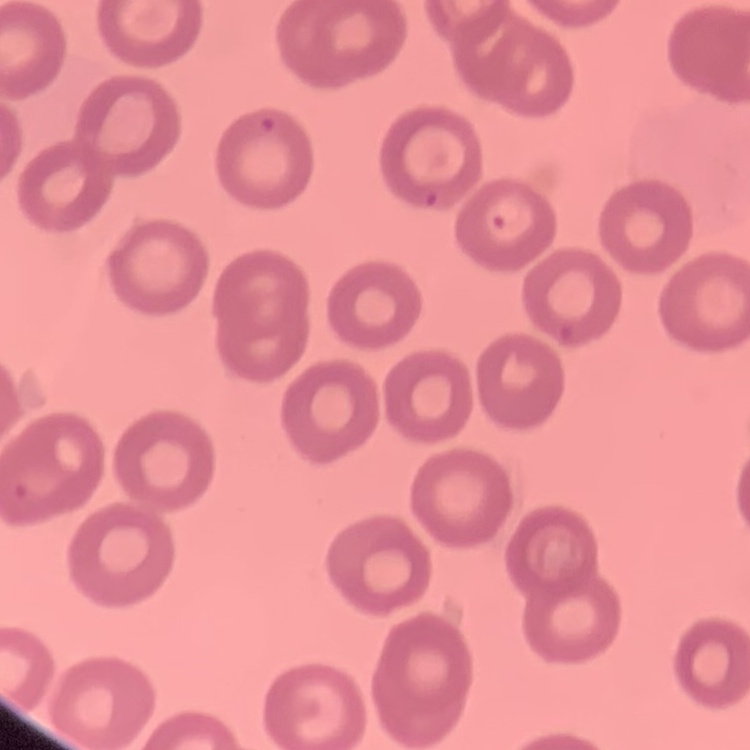
The red blood cells show no rouleaux formation. Thin blood smear. Square crop of a larger photomicrograph. Stained with either Field's or Giemsa.